Identify the preparation type.
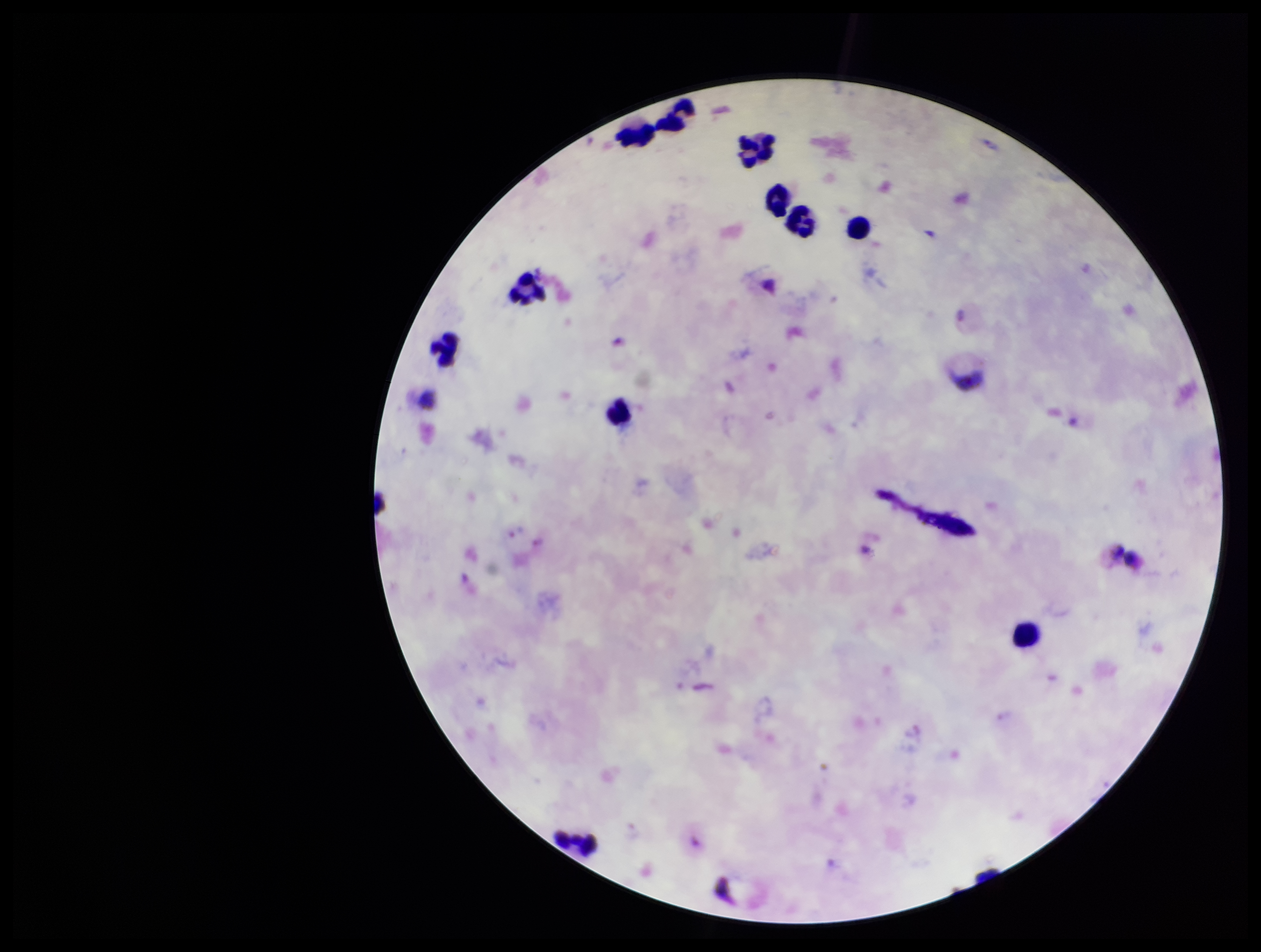
It is a thick blood smear.

capture = smartphone photograph through the microscope eyepiece
Plasmodium parasites = none seen
parasite count = 0
patient malaria status = positive
leukocyte count = 10
stain = Giemsa
field of view = single
species reported for this patient = Plasmodium vivax
image size = 1261×952 pixels